Locate every uninfected red blood cell.
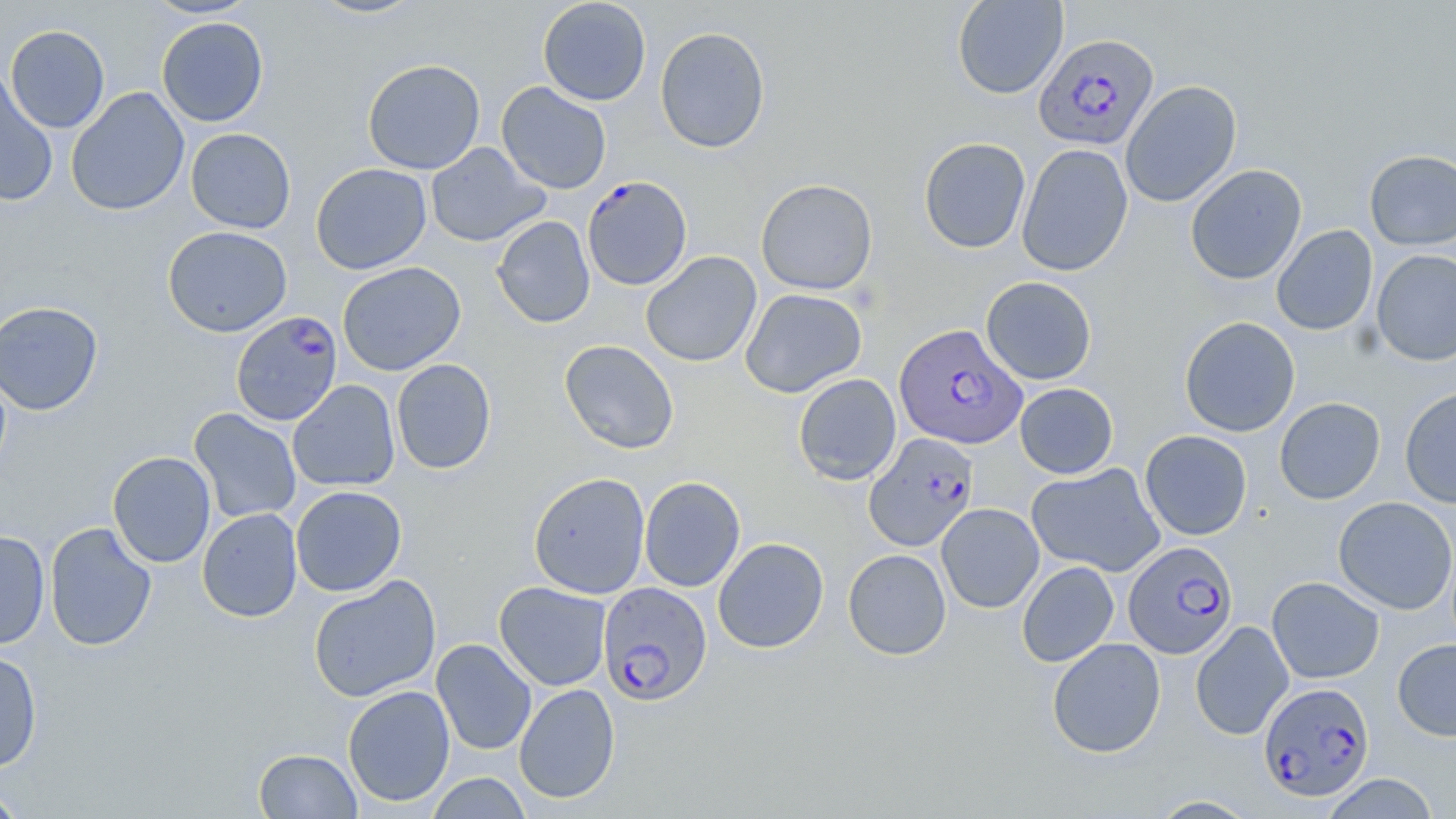

Approximate bounding boxes as (x1, y1, x2, y2) in pixels.
Uninfected red blood cells: (143, 0, 261, 19), (307, 0, 427, 20), (537, 0, 651, 106), (952, 0, 1068, 99), (156, 16, 269, 127), (5, 25, 110, 133), (655, 26, 770, 154), (362, 58, 485, 175), (0, 70, 58, 206), (1121, 80, 1242, 207), (496, 81, 612, 194), (65, 87, 190, 216), (185, 128, 296, 233), (919, 137, 1031, 254), (425, 142, 548, 247), (1016, 143, 1133, 276), (1364, 149, 1456, 250), (311, 163, 432, 275), (1185, 164, 1307, 284), (755, 178, 878, 295), (491, 215, 595, 328), (1272, 224, 1378, 336), (162, 225, 293, 337), (1371, 249, 1456, 366), (641, 251, 762, 368), (337, 262, 466, 376), (981, 276, 1097, 385), (740, 288, 867, 397), (0, 301, 104, 416), (1179, 316, 1300, 437), (559, 339, 679, 454), (391, 358, 496, 474), (793, 373, 901, 485), (287, 379, 400, 491), (1014, 383, 1118, 479), (1400, 386, 1456, 508), (1274, 397, 1385, 504), (188, 408, 302, 524), (1139, 430, 1252, 540), (108, 451, 216, 568), (1026, 462, 1166, 577), (528, 472, 651, 599), (639, 476, 746, 592), (290, 485, 407, 596), (1333, 496, 1456, 615), (936, 503, 1044, 613), (197, 507, 302, 622), (44, 522, 157, 651), (0, 530, 50, 651), (713, 537, 829, 653), (843, 548, 951, 660), (1017, 561, 1119, 667), (307, 575, 441, 703), (1266, 577, 1384, 684), (494, 581, 612, 691), (1190, 621, 1293, 740), (1047, 637, 1166, 758), (431, 638, 537, 755), (1392, 638, 1456, 741), (0, 649, 43, 772), (514, 683, 620, 804), (342, 685, 455, 807), (253, 748, 362, 818), (424, 772, 532, 818), (1320, 773, 1440, 818), (0, 785, 28, 818), (1148, 795, 1260, 818).

Summary:
  - Plasmodium falciparum-infected red blood cell locations: (1034, 33, 1159, 151), (582, 175, 692, 291), (230, 309, 343, 426), (894, 324, 1027, 449), (864, 432, 979, 552), (1124, 541, 1238, 659), (597, 582, 712, 705), (1259, 682, 1374, 802)
  - Slide-level diagnosis: Plasmodium falciparum
  - Magnification: 1000x
  - Preparation: thin blood smear
  - Stain: May-Grünwald-Giemsa
  - Field of view: single
  - Modality: optical microscopy
  - Image size: 1456×819 pixels